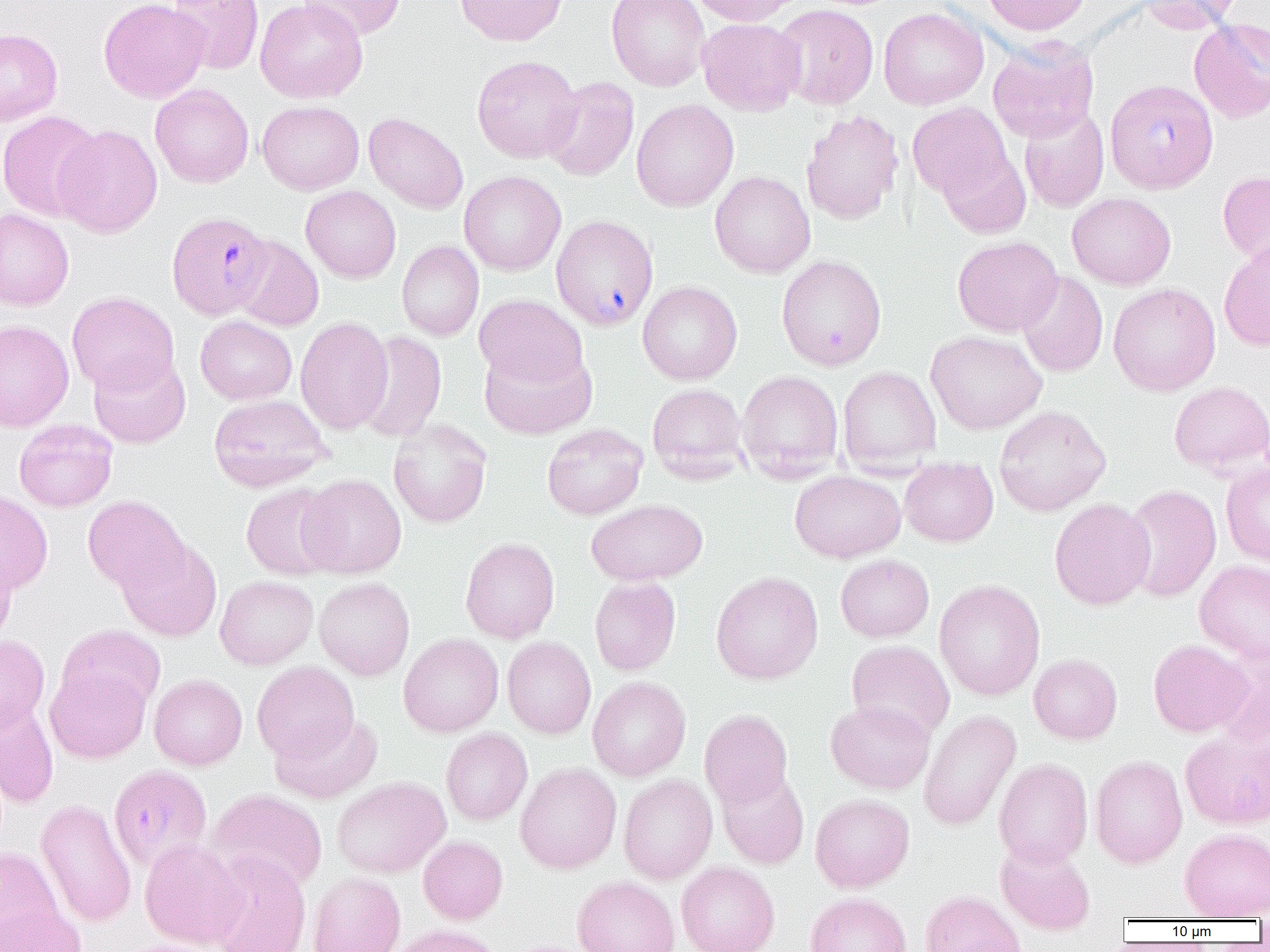
slide_level_diagnosis: Plasmodium falciparum
field_of_view: single
image_size: 1270×952 pixels
modality: light microscopy
uninfected_red_blood_cell_locations: 'approximate bounding boxes as (x1, y1, x2, y2) in pixels: (98, 0, 209, 104), (167, 0, 264, 75), (255, 0, 368, 104), (297, 0, 406, 41), (455, 0, 567, 46), (606, 0, 710, 91), (690, 0, 805, 26), (981, 0, 1091, 36), (1134, 0, 1241, 33), (773, 4, 879, 109), (878, 7, 989, 110), (697, 17, 805, 116), (1189, 18, 1270, 123), (0, 28, 63, 126), (987, 37, 1099, 142), (471, 55, 582, 163), (542, 76, 640, 182), (150, 84, 254, 188), (631, 99, 739, 212), (257, 101, 364, 194), (907, 102, 1013, 202), (1019, 105, 1109, 213), (800, 110, 904, 226), (0, 111, 105, 221), (363, 112, 469, 214), (54, 124, 163, 238), (938, 147, 1031, 239), (1218, 170, 1270, 268), (458, 171, 566, 276), (710, 171, 816, 278), (301, 185, 401, 283), (1067, 193, 1176, 290), (0, 208, 74, 311), (233, 236, 324, 332), (952, 236, 1063, 336), (1218, 239, 1270, 352), (397, 241, 484, 341), (776, 255, 887, 370), (1017, 271, 1108, 377), (637, 281, 742, 385), (1108, 283, 1221, 396), (67, 291, 179, 395), (474, 294, 588, 391), (195, 315, 297, 405), (295, 316, 393, 435), (0, 319, 74, 432), (355, 330, 448, 443), (925, 330, 1047, 434), (479, 343, 597, 439), (88, 352, 191, 448), (837, 366, 941, 474), (736, 370, 844, 482), (1168, 381, 1270, 475), (647, 383, 749, 482), (208, 394, 331, 492), (993, 405, 1111, 516), (389, 418, 492, 528), (14, 419, 117, 512), (542, 423, 647, 520), (899, 457, 998, 547), (1221, 459, 1270, 566), (789, 470, 906, 563), (298, 474, 407, 579), (240, 482, 342, 580), (1122, 484, 1222, 603), (0, 490, 53, 594), (83, 495, 188, 593), (1049, 498, 1155, 610), (586, 499, 708, 585), (116, 536, 222, 642), (460, 537, 560, 644), (0, 550, 18, 645), (835, 554, 934, 642), (1194, 560, 1270, 664), (710, 571, 823, 685), (215, 575, 318, 669), (589, 575, 681, 676), (314, 577, 415, 680), (934, 579, 1045, 701), (57, 624, 165, 715), (398, 633, 504, 738), (0, 635, 50, 732), (502, 637, 596, 739), (1148, 639, 1253, 737), (846, 640, 955, 741), (1212, 645, 1270, 753), (1029, 654, 1122, 744), (251, 661, 359, 762), (45, 664, 150, 763), (149, 674, 247, 770), (587, 676, 691, 781), (0, 698, 59, 808), (825, 700, 934, 794), (699, 709, 793, 809), (918, 709, 1021, 831), (270, 712, 382, 804), (1180, 726, 1270, 830), (441, 728, 533, 825), (1089, 755, 1188, 869), (993, 757, 1093, 868), (515, 762, 621, 874), (716, 768, 809, 869), (618, 774, 718, 884), (331, 776, 450, 878), (207, 789, 328, 895), (810, 793, 914, 893), (35, 799, 136, 928), (1179, 828, 1270, 920), (418, 836, 508, 925), (139, 838, 246, 949), (995, 840, 1096, 934), (0, 847, 64, 948), (205, 852, 312, 952), (676, 861, 779, 952), (308, 872, 406, 952), (572, 876, 680, 952), (920, 890, 1026, 952), (805, 892, 911, 952), (0, 902, 86, 952), (389, 924, 506, 952), (118, 939, 229, 952)'
magnification: 1000x
plasmodium_falciparum_infected_red_blood_cell_locations: 'approximate bounding boxes as (x1, y1, x2, y2) in pixels: (1105, 78, 1219, 194), (171, 209, 278, 318), (551, 216, 659, 331), (107, 762, 211, 871)'
preparation: thin blood smear